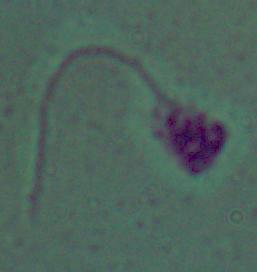

Summary:
  - Modality: micrograph
  - Magnification: 1000x
  - Identification: Leishmania